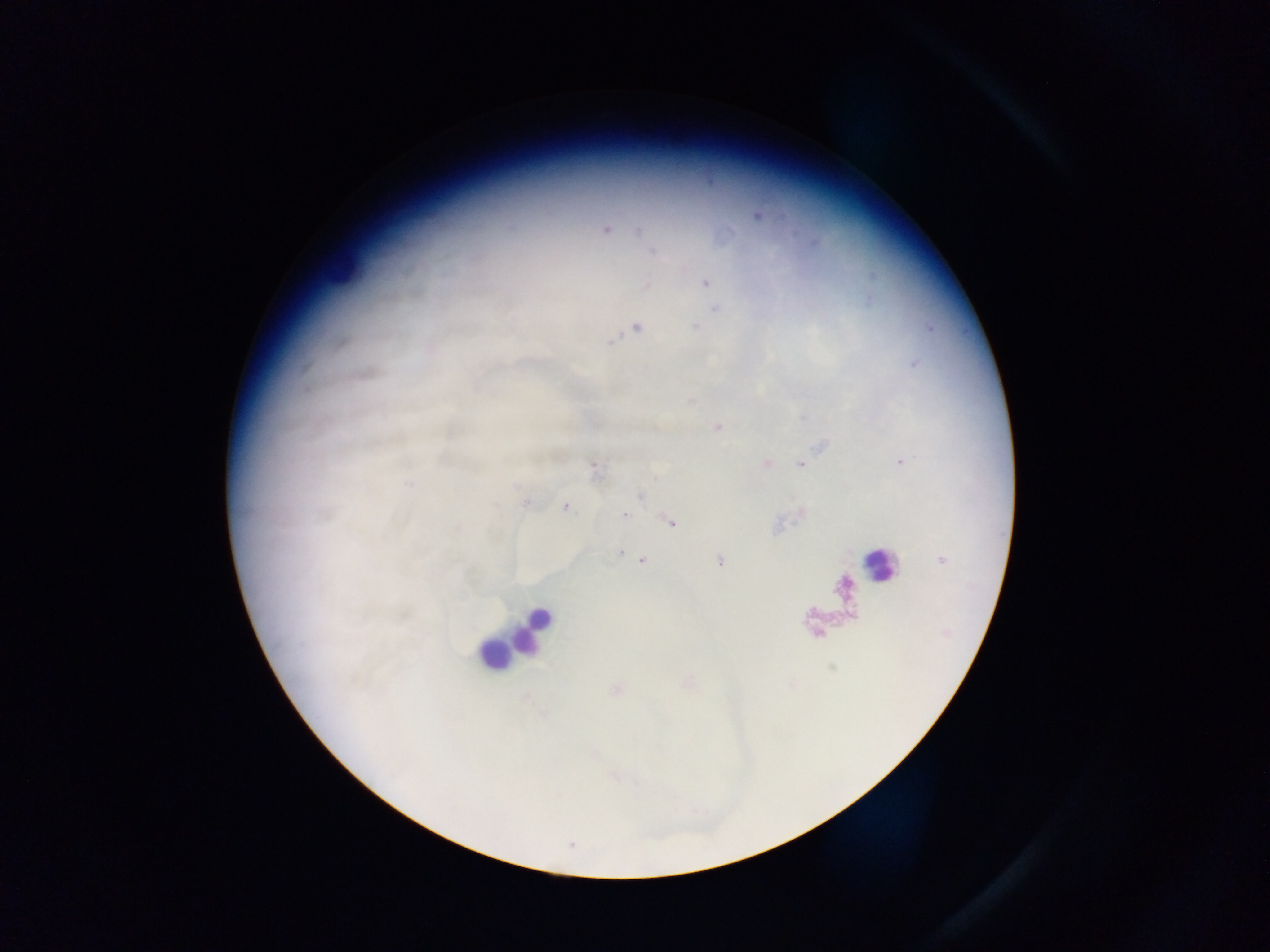

preparation = thick blood smear
Plasmodium parasite locations = approximate centers as [x, y] in pixels: [757, 215], [606, 229], [639, 231], [653, 252], [705, 282], [646, 285], [715, 308], [636, 327], [696, 327], [610, 341], [716, 427], [901, 462], [801, 463], [767, 464], [594, 469], [408, 484], [640, 495], [526, 503], [565, 507], [625, 515], [671, 523], [620, 553], [631, 557], [643, 560], [719, 562], [617, 689]
image size = 1270×952 pixels
leukocyte locations = approximate centers as [x, y] in pixels: [342, 264], [877, 565], [531, 627], [492, 655]
capture = mobile-phone photograph through a microscope
country = Ghana
field of view = single